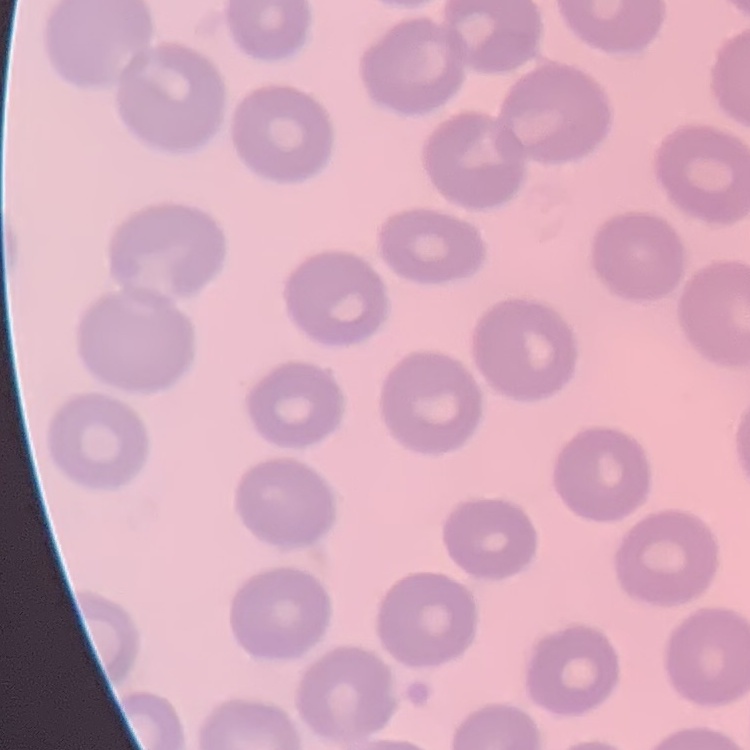
red blood cell morphology = no rouleaux formation
preparation = thin blood film
stain = Field's or Giemsa
image type = square crop of a larger photomicrograph